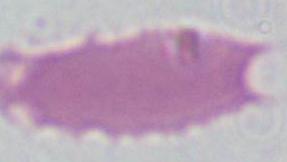
identification = red blood cell
magnification = 1000x
modality = photomicrograph